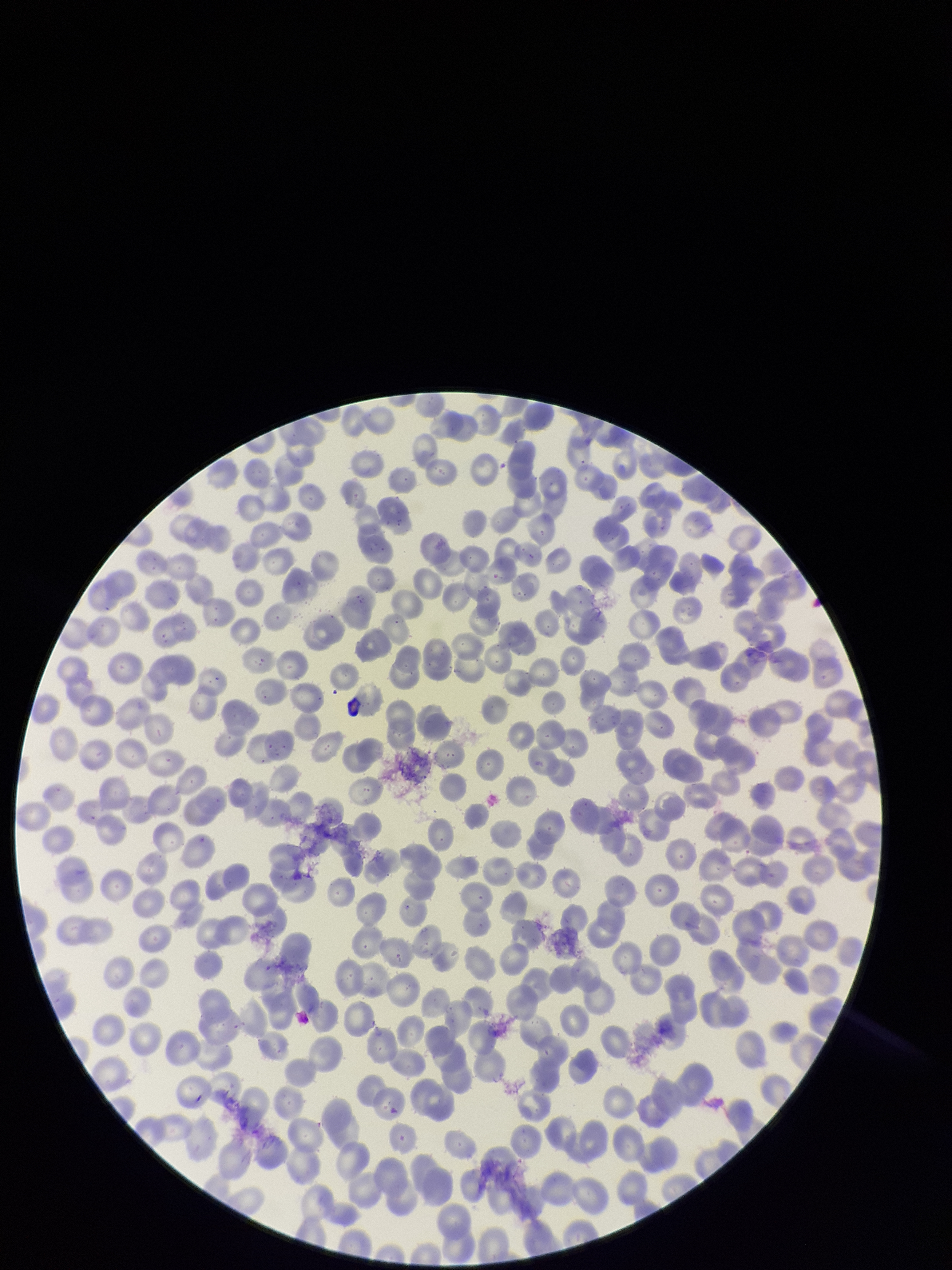

field of view = single
image size = 952×1270 pixels
red blood cell count = 329
parasitized red blood cells = none seen
capture = smartphone photograph through the microscope eyepiece
species reported for this patient = Plasmodium falciparum
preparation = thin
patient malaria status = infected
stain = Giemsa
parasitized red blood cell count = 0